Describe the morphology of the red blood cells.
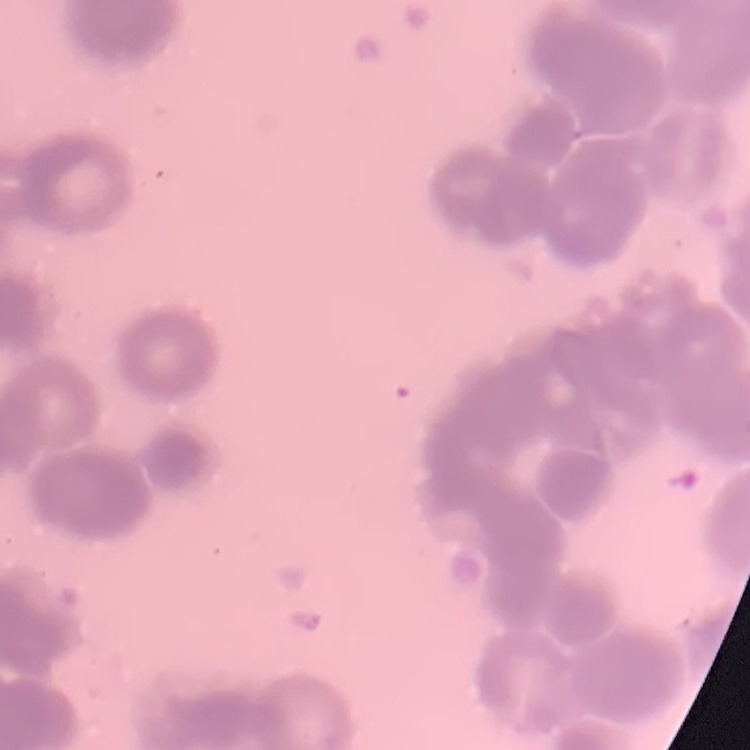
They show rouleaux formation.

Thin peripheral smear. Square crop of a larger photomicrograph. Field's or Giemsa stain.